Describe the morphology of the red blood cells.
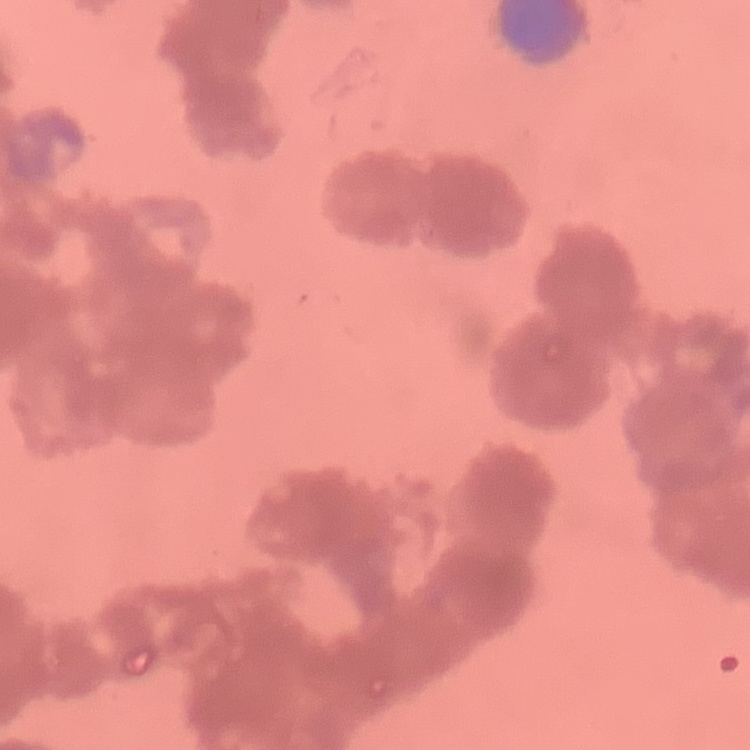
Rouleaux formation.

Summary:
  - Image type: one tile cut from a larger photomicrograph
  - Preparation: thin blood smear
  - Stain: Field's or Giemsa